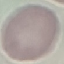

Summary:
  - Malaria status: uninfected
  - Image type: cell patch, automatically extracted from a larger field of view and resized to 64 × 64 pixels
  - Stain: Giemsa
  - Capture: smartphone camera at the microscope eyepiece
  - Preparation: thin blood smear